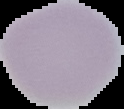
image_size: 124×109 pixels
image_type: segmented cell region with the area outside set to black
malaria_status: uninfected
preparation: thin blood smear